Report the malaria status of this cell.
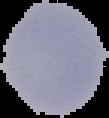
Uninfected.

Summary:
  - Image size: 109×118 pixels
  - Preparation: thin blood film
  - Image type: segmented cell region with the area outside set to black